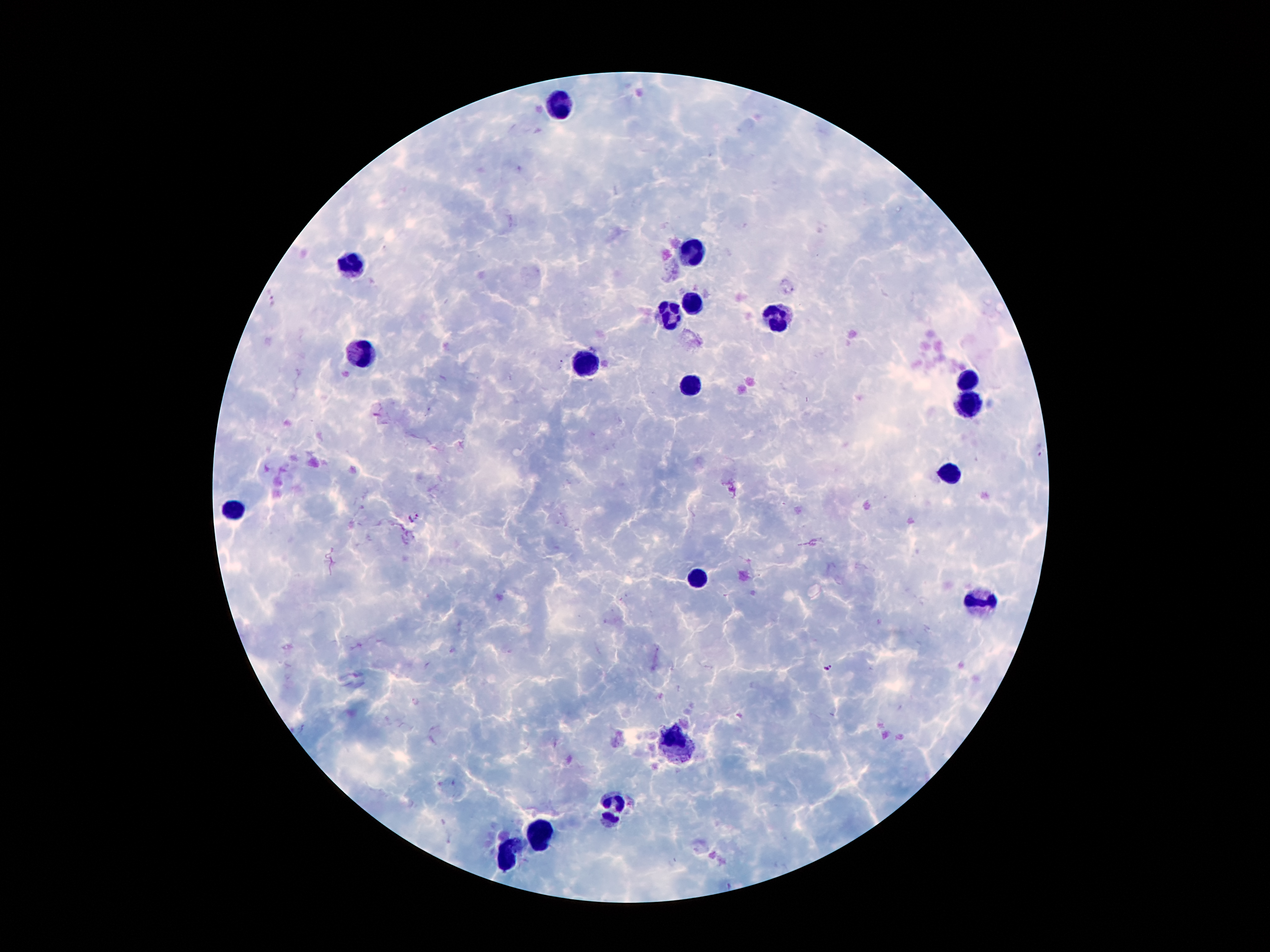
Approximate centers as [x, y] in pixels.
Summary:
  - Leukocyte locations: [560, 103], [693, 254], [352, 268], [693, 296], [673, 314], [779, 320], [365, 354], [580, 367], [969, 375], [690, 384], [963, 410], [954, 471], [236, 509], [699, 577], [983, 601], [676, 743], [613, 810], [538, 833], [511, 853]
  - Plasmodium parasite locations: [414, 517], [828, 668]
  - Magnification: 100x
  - Patient malaria status: infected with Plasmodium falciparum
  - Preparation: thick blood smear
  - Capture: smartphone through the microscope eyepiece
  - Stain: Giemsa
  - Field of view: single
  - Image size: 1270×952 pixels